State which cell type is depicted.
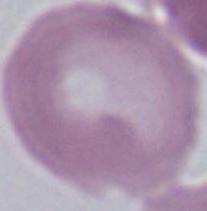
An erythrocyte.

Captured at 1000x magnification. Photomicrograph.